State which parasite is depicted.
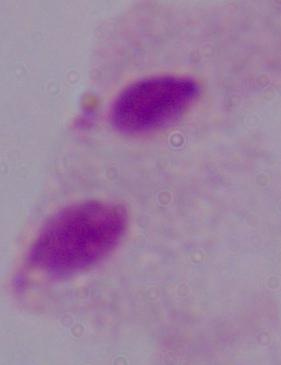
A trichomonad.

Summary:
  - Magnification: 1000x
  - Modality: micrograph